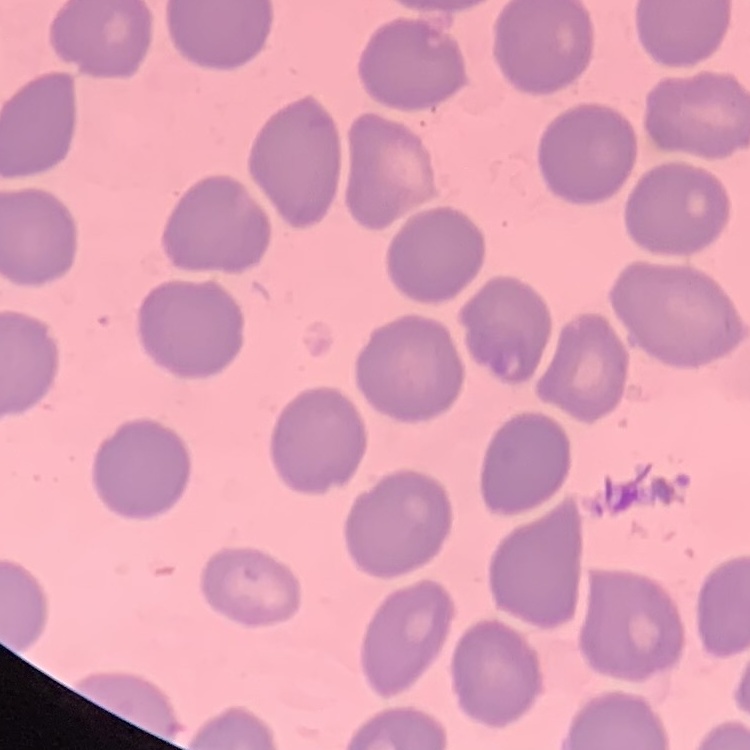

Summary:
  - Erythrocyte morphology: no rouleaux formation
  - Preparation: thin peripheral smear
  - Stain: Field's or Giemsa
  - Image type: square crop of a larger photomicrograph